Assess the morphology of the erythrocytes.
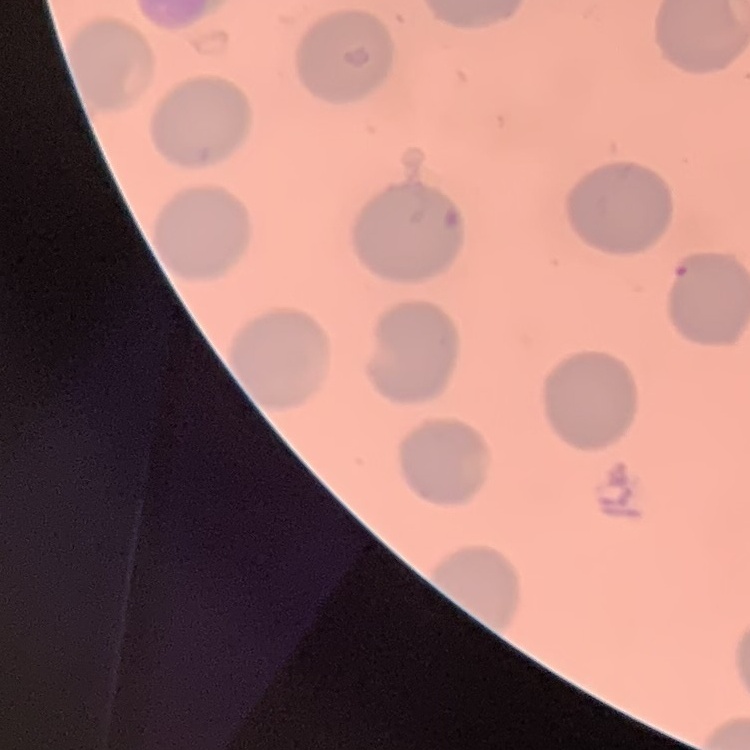
No rouleaux formation.

Summary:
  - Stain: Field's or Giemsa
  - Image type: one tile cut from a larger photomicrograph
  - Preparation: thin blood smear